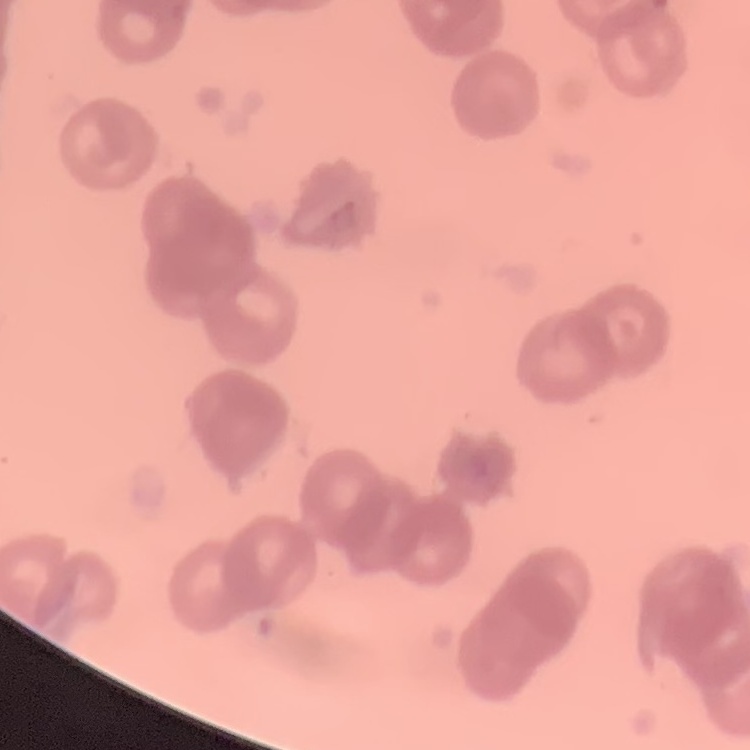 The erythrocytes show rouleaux formation. Stained with either Field's or Giemsa. Thin blood smear. Square crop of a larger photomicrograph.